Comment on the morphology of the red blood cells.
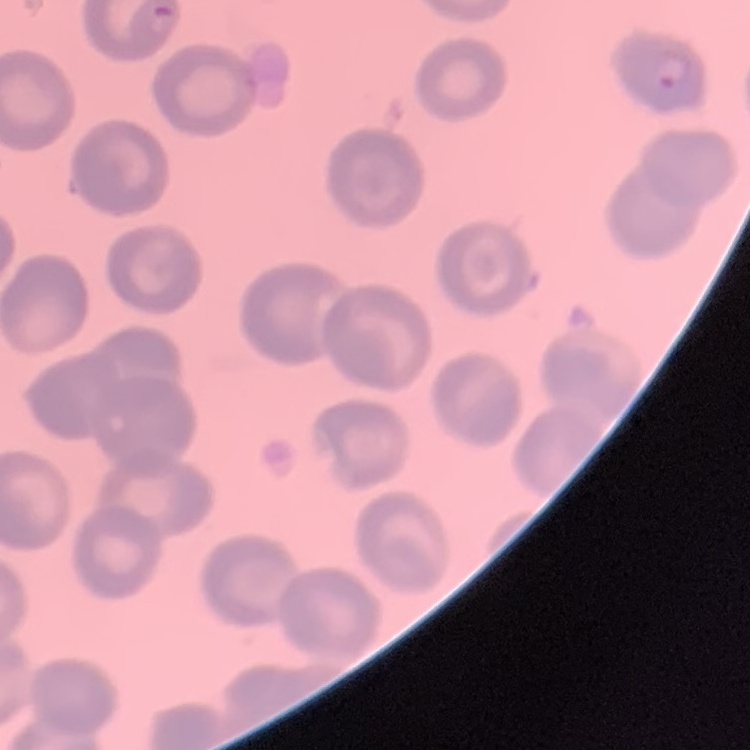
They show no rouleaux formation.

Summary:
  - Image type: square crop of a larger photomicrograph
  - Stain: Field's or Giemsa
  - Preparation: thin blood film